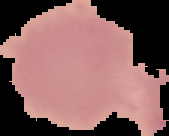

{
  "image_type": "segmented cell region with the area outside set to black",
  "image_size": "169×136 pixels",
  "preparation": "thin blood smear",
  "malaria_status": "uninfected"
}